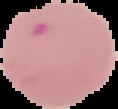

Summary:
  - Preparation: thin blood smear
  - Image type: cell region segmented out of the field of view; surrounding area masked to black
  - Image size: 118×109 pixels
  - Result: malaria parasites detected